Identify the blood parasite species.
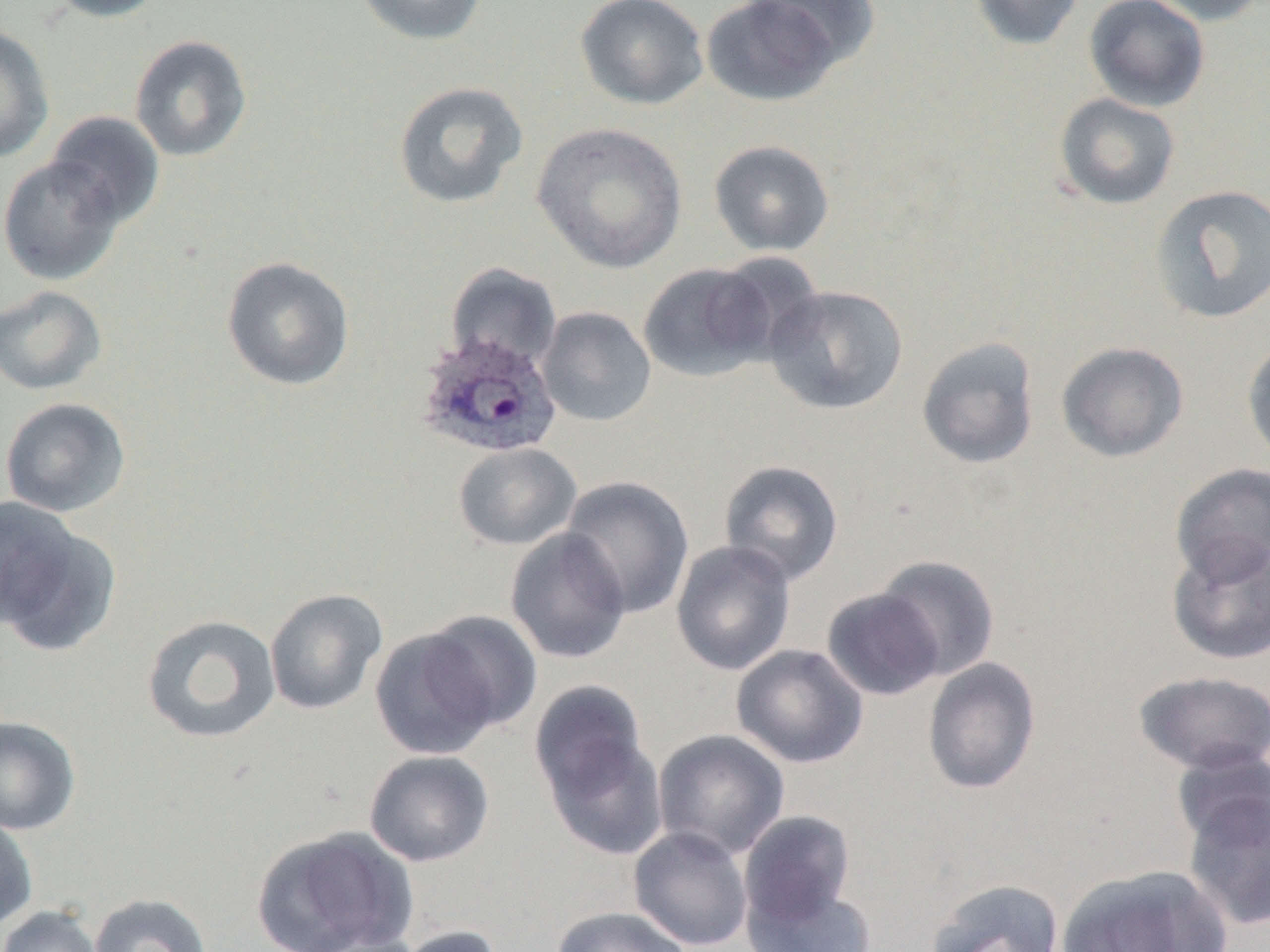
Plasmodium ovale.

Summary:
  - Coordinate format: approximate bounding boxes as [x1, y1, x2, y2] in pixels
  - Plasmodium ovale-infected red blood cell locations: [414, 330, 562, 460]
  - Uninfected red blood cell locations: [43, 0, 168, 22], [351, 0, 487, 46], [574, 0, 709, 110], [751, 0, 880, 70], [968, 0, 1086, 51], [1084, 0, 1210, 112], [1139, 0, 1268, 26], [701, 1, 841, 107], [0, 26, 55, 163], [128, 34, 253, 162], [392, 80, 529, 209], [1053, 93, 1181, 210], [45, 111, 165, 229], [532, 122, 687, 273], [708, 139, 835, 256], [0, 155, 125, 285], [1150, 184, 1270, 325], [221, 256, 356, 391], [637, 262, 777, 382], [445, 263, 562, 373], [764, 284, 909, 415], [0, 285, 108, 395], [537, 306, 656, 427], [1242, 335, 1270, 469], [916, 336, 1040, 470], [1056, 341, 1189, 463], [0, 397, 132, 517], [453, 442, 581, 551], [718, 459, 844, 586], [1170, 463, 1270, 585], [559, 476, 695, 619], [0, 496, 103, 647], [505, 527, 632, 664], [1166, 533, 1270, 666], [671, 539, 796, 676], [874, 554, 1001, 680], [821, 587, 945, 701], [264, 588, 388, 715], [420, 610, 543, 732], [141, 614, 282, 744], [369, 624, 504, 760], [731, 644, 869, 769], [922, 657, 1042, 795], [1133, 670, 1270, 775], [528, 679, 656, 823], [0, 715, 81, 835], [652, 728, 790, 861], [1170, 747, 1269, 851], [363, 749, 495, 867], [1182, 788, 1269, 931], [738, 809, 857, 930], [0, 813, 38, 931], [251, 825, 418, 952], [628, 826, 754, 951], [1057, 864, 1231, 952], [925, 877, 1064, 952], [745, 880, 877, 952], [87, 892, 213, 952], [0, 905, 104, 952], [551, 906, 692, 952], [390, 925, 508, 952]
  - Modality: light microscopy
  - Magnification: 1000x
  - Preparation: thin blood smear
  - Image size: 1270×952 pixels
  - Field of view: one of a larger specimen